Name the blood parasite species.
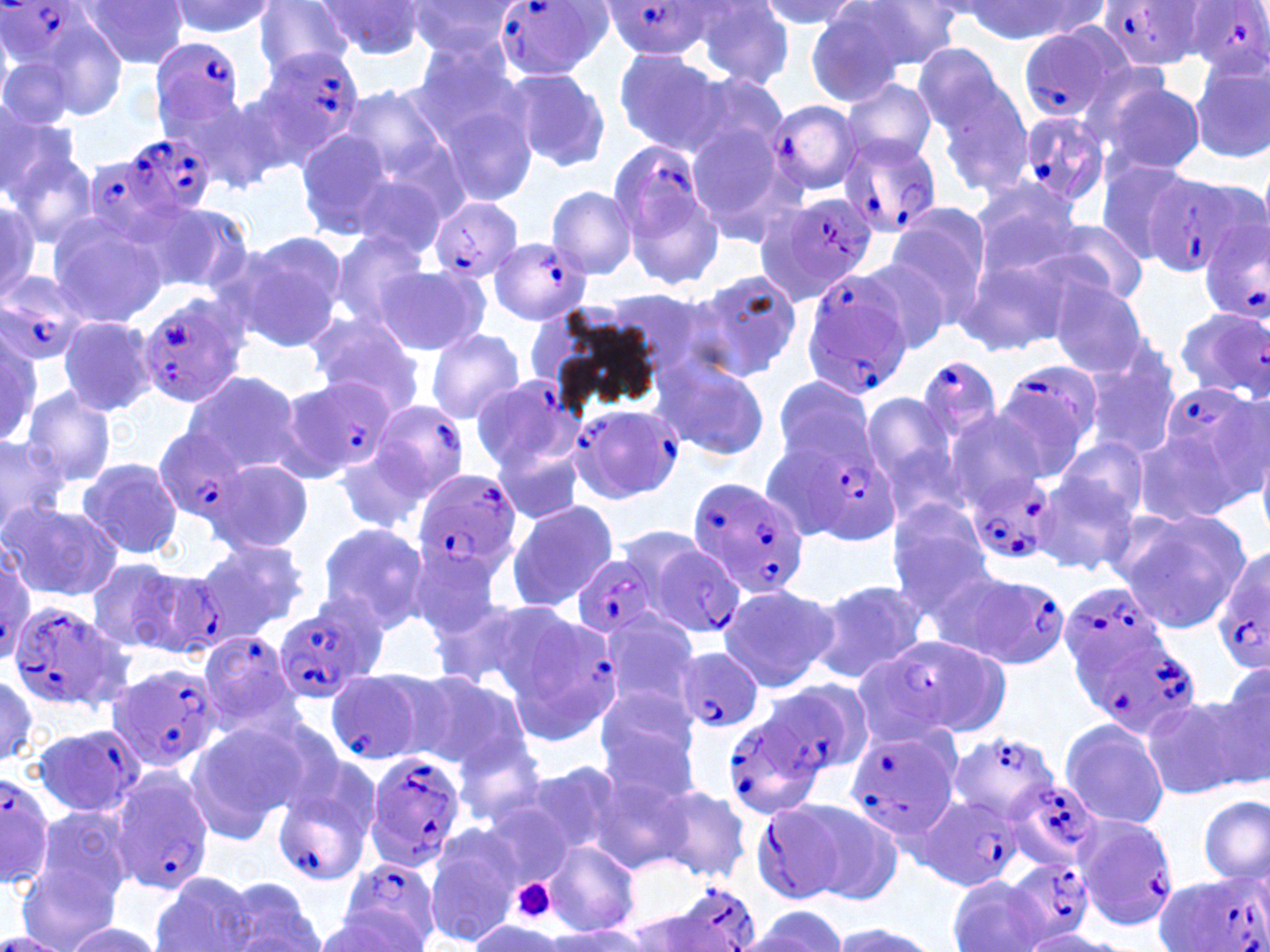

Plasmodium falciparum.

preparation = thin blood film
field of view = one of a larger specimen
magnification = 1000x
Plasmodium falciparum-infected red blood cell locations (subset) = approximate bounding boxes as [x1, y1, x2, y2] in pixels: [1101, 0, 1210, 68], [0, 1, 98, 75], [490, 1, 611, 82], [600, 1, 716, 60], [1187, 1, 1270, 79], [1016, 23, 1125, 126], [150, 37, 248, 132], [252, 47, 365, 154], [765, 99, 866, 196], [1013, 111, 1112, 214], [88, 130, 221, 247], [839, 135, 943, 238], [605, 140, 722, 246], [1143, 177, 1258, 278], [766, 190, 878, 300], [430, 197, 524, 283], [1199, 214, 1270, 328], [488, 236, 591, 327], [0, 271, 90, 365], [798, 271, 912, 402], [138, 294, 250, 408], [1172, 306, 1269, 402], [912, 353, 1006, 449], [994, 360, 1104, 472], [282, 374, 398, 481], [469, 376, 579, 473], [1157, 377, 1267, 496], [364, 401, 471, 511], [569, 402, 684, 505], [154, 428, 248, 525], [811, 450, 901, 545], [412, 468, 521, 580], [966, 471, 1056, 567], [686, 476, 809, 598], [640, 538, 747, 641], [1213, 544, 1270, 673], [572, 554, 666, 638], [1, 555, 38, 663], [129, 566, 229, 657], [944, 569, 1072, 672], [1058, 580, 1172, 684], [8, 602, 134, 715], [274, 603, 382, 705], [523, 605, 623, 733], [197, 630, 301, 739], [1076, 630, 1199, 741], [891, 636, 1012, 736], [848, 648, 961, 748], [103, 662, 222, 776], [324, 667, 442, 766], [768, 680, 874, 776], [723, 712, 828, 820], [30, 724, 145, 818], [843, 728, 958, 840], [950, 731, 1062, 825], [364, 750, 467, 871], [270, 758, 382, 886], [107, 770, 216, 895], [0, 773, 56, 889], [1009, 778, 1102, 870], [921, 796, 1027, 891], [752, 801, 852, 904], [1072, 812, 1177, 931], [338, 854, 442, 949], [1154, 872, 1269, 952], [656, 880, 761, 952], [0, 930, 70, 951]
image size = 1270×952 pixels
modality = light microscopy
stain = May-Grünwald-Giemsa
platelet locations = approximate bounding boxes as [x1, y1, x2, y2] in pixels: [510, 877, 556, 924]
uninfected red blood cell locations (subset) = approximate bounding boxes as [x1, y1, x2, y2] in pixels: [79, 0, 191, 69], [756, 0, 863, 32], [849, 0, 964, 72], [165, 1, 278, 38], [318, 1, 425, 60], [404, 1, 518, 60], [969, 1, 1106, 43], [253, 2, 355, 76], [690, 2, 795, 88], [805, 7, 913, 107], [25, 14, 129, 122], [910, 42, 1013, 141], [412, 48, 537, 197], [612, 50, 728, 155], [0, 54, 76, 139], [1186, 55, 1270, 162], [507, 69, 610, 173], [686, 71, 788, 161], [931, 76, 1035, 201], [840, 77, 937, 166], [1097, 79, 1206, 177], [333, 81, 467, 211], [166, 91, 279, 195], [0, 105, 79, 207], [686, 123, 795, 241], [294, 126, 396, 238], [5, 144, 96, 249], [340, 152, 462, 262], [1095, 159, 1184, 265], [970, 175, 1084, 272], [546, 185, 638, 279], [0, 192, 43, 304], [140, 200, 253, 292], [881, 206, 992, 328], [45, 213, 168, 327], [1040, 218, 1150, 309], [330, 229, 432, 331], [234, 232, 348, 352], [958, 242, 1095, 358], [855, 257, 958, 355], [376, 267, 486, 353], [696, 270, 802, 378], [1052, 280, 1150, 376], [604, 287, 727, 390], [305, 313, 423, 414], [57, 315, 159, 417], [0, 325, 43, 448], [425, 329, 524, 423], [1079, 342, 1180, 460], [655, 359, 768, 461], [182, 370, 303, 477], [768, 376, 878, 477], [20, 386, 118, 487], [859, 394, 962, 505], [940, 409, 1051, 508], [1131, 431, 1240, 526], [0, 434, 68, 539], [1055, 437, 1151, 525], [493, 439, 586, 525], [334, 442, 435, 537], [77, 457, 184, 558], [212, 458, 313, 553], [1033, 475, 1140, 577], [506, 499, 618, 612], [3, 501, 123, 602], [885, 504, 992, 611], [1113, 507, 1252, 631], [317, 523, 428, 632], [196, 537, 310, 637], [406, 541, 504, 640], [86, 557, 189, 653], [808, 579, 929, 683], [717, 582, 837, 693], [430, 595, 560, 696], [594, 611, 701, 715], [399, 668, 528, 772], [1203, 674, 1270, 790], [594, 681, 702, 793], [1141, 695, 1253, 799], [1090, 702, 1215, 814], [1059, 718, 1171, 829], [182, 721, 302, 844], [452, 736, 547, 830], [508, 759, 622, 865], [590, 770, 698, 872], [650, 784, 753, 882], [1199, 794, 1269, 884], [785, 798, 904, 902], [32, 806, 135, 906], [423, 826, 522, 947], [539, 840, 640, 937], [16, 861, 124, 952], [151, 871, 259, 952], [946, 875, 1052, 952], [219, 879, 324, 952], [745, 907, 848, 952], [316, 909, 434, 950], [468, 916, 563, 950], [59, 921, 165, 952], [828, 921, 937, 952], [538, 927, 651, 952], [1017, 930, 1122, 951]